Report the malaria status of this cell.
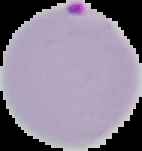

It is parasitized.

Image is 142×151 pixels. From a thin blood film. The area outside the segmented cell region is set to black.